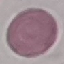
result = no malaria parasites seen
stain = Giemsa
capture = smartphone through the microscope eyepiece
image type = cell patch, automatically extracted from a larger field of view and resized to 64 × 64 pixels
preparation = thin smear